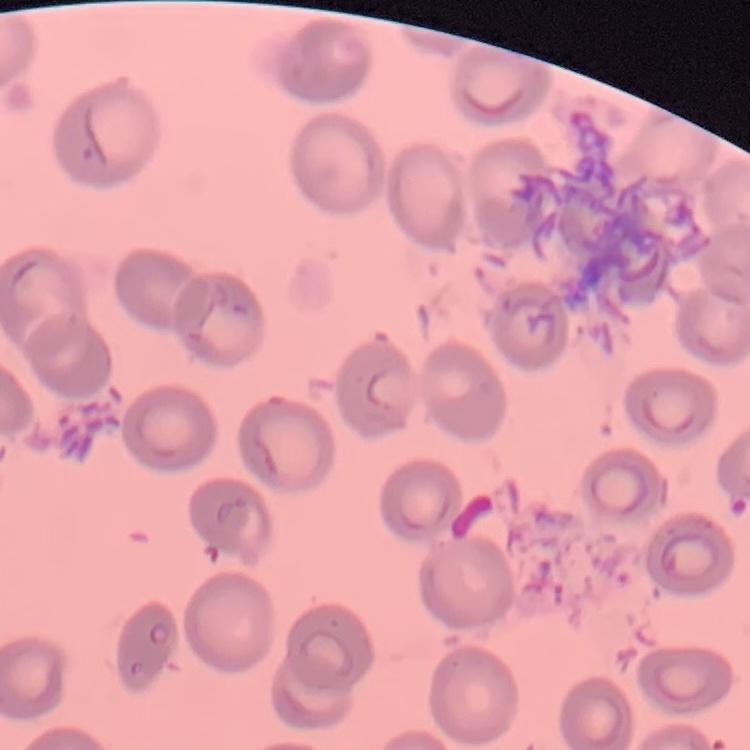 The red blood cells show no rouleaux formation. Thin blood smear. Field's or Giemsa stain. One tile cut from a larger photomicrograph.